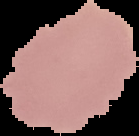

Summary:
  - Preparation: thin blood film
  - Image type: cell region segmented out of the field of view; surrounding area masked to black
  - Image size: 139×136 pixels
  - Malaria status: uninfected